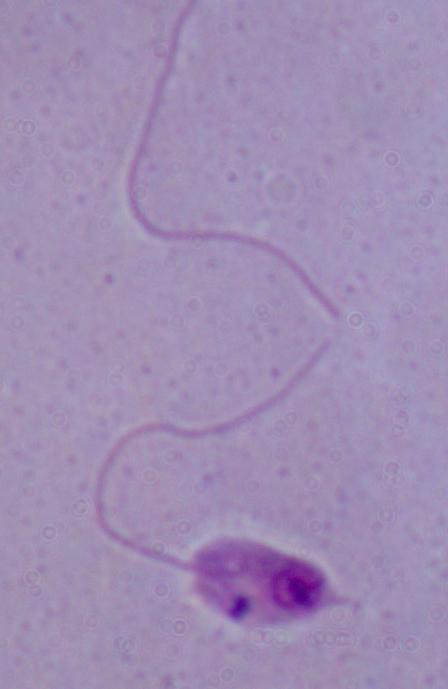
modality: micrograph
magnification: 1000x
identification: Leishmania